Describe the morphology of the red blood cells.
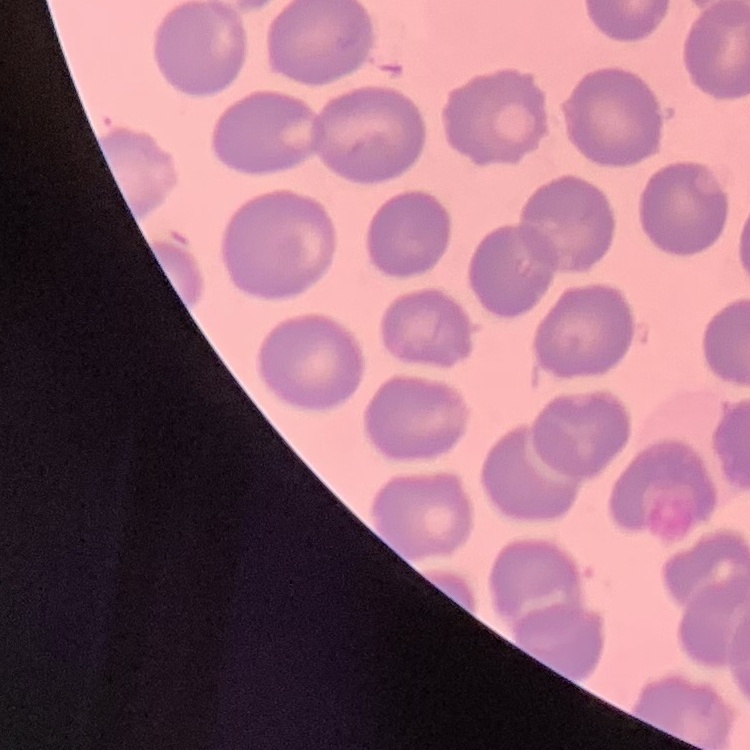
No rouleaux formation.

Thin blood film. Field's or Giemsa stain. One tile cut from a larger photomicrograph.